Outline each blood parasite and name the species.
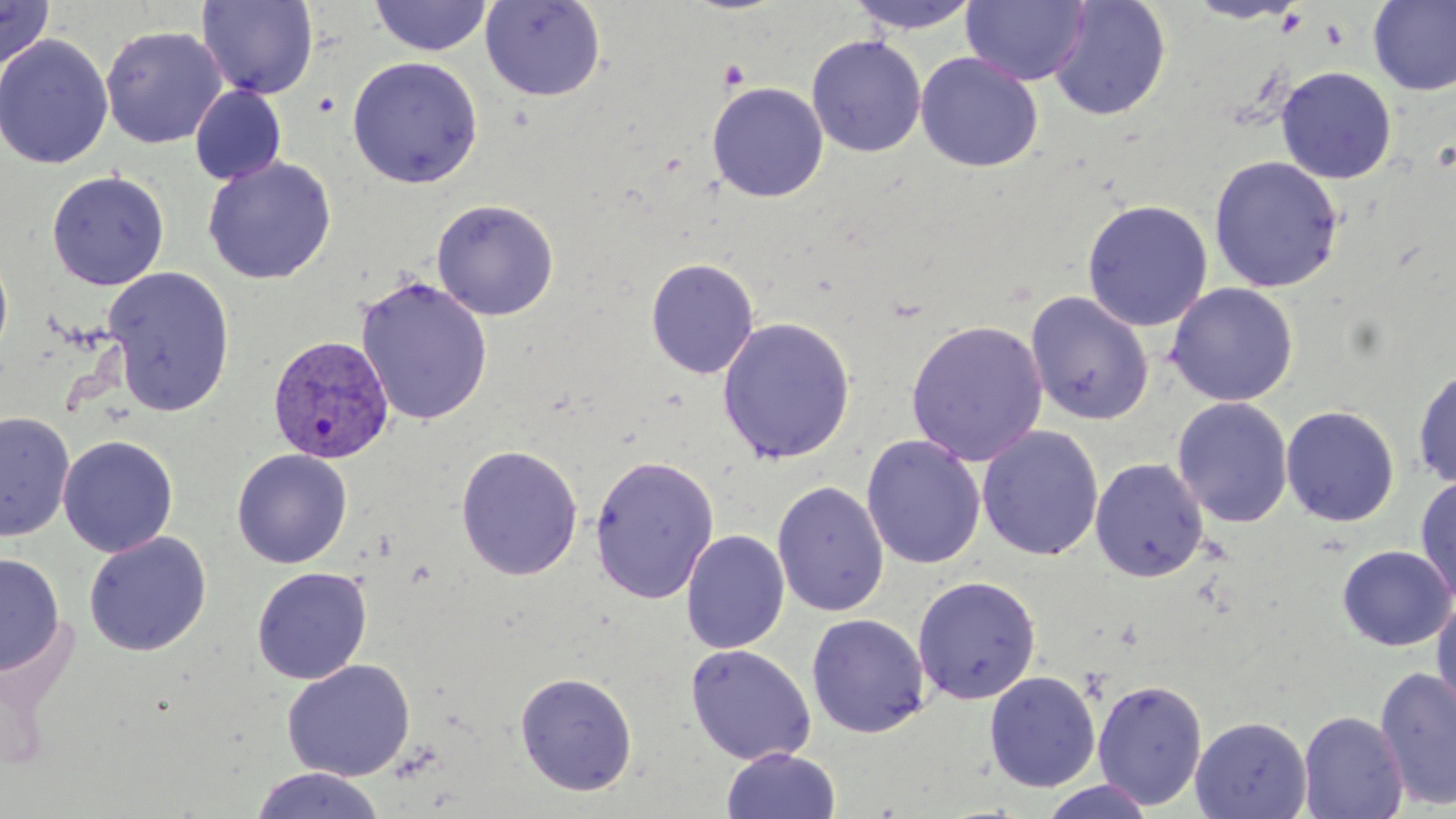
Approximate bounding boxes as named x1/y1/x2/y2 corners in pixels.
Plasmodium vivax-infected red blood cells: (x1=267, y1=334, x2=396, y2=466).
No Plasmodium falciparum, Plasmodium ovale, Plasmodium malariae, Babesia divergens, or Trypanosoma brucei observed.

Summary:
  - Uninfected red blood cell locations: (x1=0, y1=0, x2=56, y2=71), (x1=368, y1=0, x2=492, y2=57), (x1=480, y1=0, x2=606, y2=102), (x1=844, y1=0, x2=983, y2=35), (x1=1048, y1=0, x2=1172, y2=121), (x1=1185, y1=0, x2=1305, y2=24), (x1=197, y1=1, x2=319, y2=99), (x1=961, y1=1, x2=1091, y2=86), (x1=1368, y1=1, x2=1456, y2=96), (x1=101, y1=25, x2=226, y2=149), (x1=0, y1=34, x2=114, y2=171), (x1=806, y1=35, x2=927, y2=157), (x1=915, y1=52, x2=1044, y2=172), (x1=346, y1=56, x2=484, y2=189), (x1=1275, y1=66, x2=1397, y2=184), (x1=706, y1=81, x2=829, y2=203), (x1=190, y1=85, x2=287, y2=185), (x1=1208, y1=155, x2=1344, y2=293), (x1=202, y1=156, x2=337, y2=285), (x1=47, y1=170, x2=169, y2=290), (x1=431, y1=198, x2=559, y2=320), (x1=1082, y1=199, x2=1214, y2=332), (x1=0, y1=248, x2=13, y2=365), (x1=645, y1=258, x2=759, y2=379), (x1=102, y1=266, x2=236, y2=416), (x1=355, y1=276, x2=493, y2=426), (x1=1166, y1=282, x2=1299, y2=406), (x1=1025, y1=291, x2=1154, y2=426), (x1=716, y1=316, x2=856, y2=466), (x1=905, y1=318, x2=1048, y2=467), (x1=1413, y1=365, x2=1456, y2=490), (x1=1172, y1=396, x2=1293, y2=528), (x1=1281, y1=405, x2=1400, y2=527), (x1=0, y1=412, x2=74, y2=543), (x1=977, y1=424, x2=1104, y2=561), (x1=58, y1=435, x2=179, y2=557), (x1=862, y1=435, x2=986, y2=570), (x1=456, y1=444, x2=583, y2=581), (x1=232, y1=449, x2=353, y2=569), (x1=589, y1=454, x2=720, y2=604), (x1=1090, y1=458, x2=1209, y2=581), (x1=1414, y1=474, x2=1456, y2=605), (x1=772, y1=481, x2=889, y2=618), (x1=681, y1=530, x2=790, y2=654), (x1=84, y1=531, x2=211, y2=656), (x1=1336, y1=544, x2=1456, y2=651), (x1=0, y1=553, x2=65, y2=677), (x1=252, y1=567, x2=372, y2=684), (x1=912, y1=575, x2=1041, y2=705), (x1=1431, y1=595, x2=1456, y2=722), (x1=806, y1=613, x2=930, y2=739), (x1=685, y1=644, x2=816, y2=765), (x1=281, y1=659, x2=415, y2=781), (x1=1374, y1=666, x2=1456, y2=810), (x1=984, y1=670, x2=1102, y2=792), (x1=515, y1=672, x2=638, y2=796), (x1=1092, y1=678, x2=1208, y2=810), (x1=1298, y1=710, x2=1409, y2=819), (x1=1190, y1=716, x2=1312, y2=818), (x1=721, y1=748, x2=841, y2=819), (x1=250, y1=767, x2=385, y2=819), (x1=1038, y1=778, x2=1156, y2=819)
  - Slide-level diagnosis: Plasmodium vivax
  - Magnification: 1000x
  - Modality: optical microscopy
  - Stain: May-Grünwald-Giemsa
  - Preparation: thin blood smear
  - Image size: 1456×819 pixels
  - Field of view: one of a larger specimen